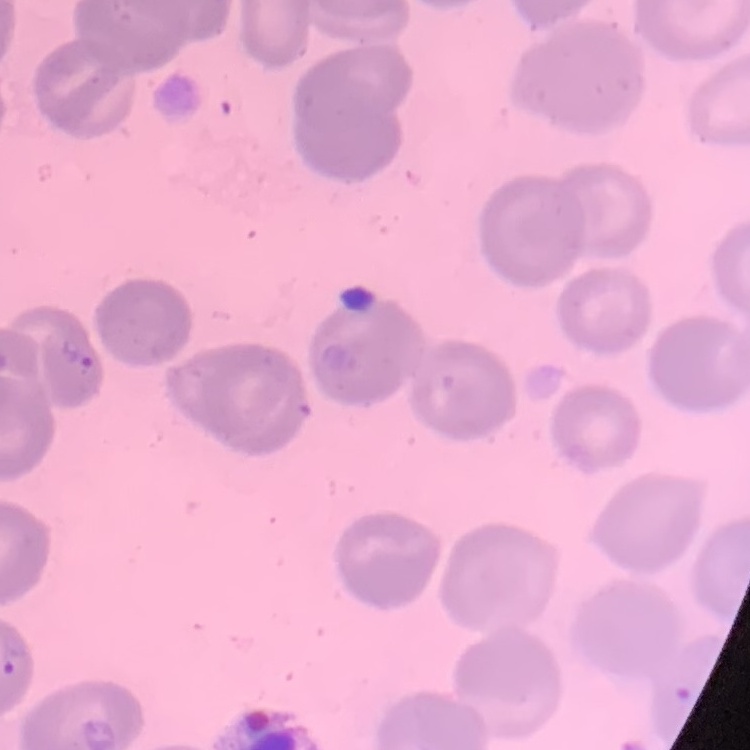
Summary:
  - Red blood cell morphology: no rouleaux formation
  - Stain: Field's or Giemsa
  - Image type: square crop of a larger photomicrograph
  - Preparation: thin blood smear